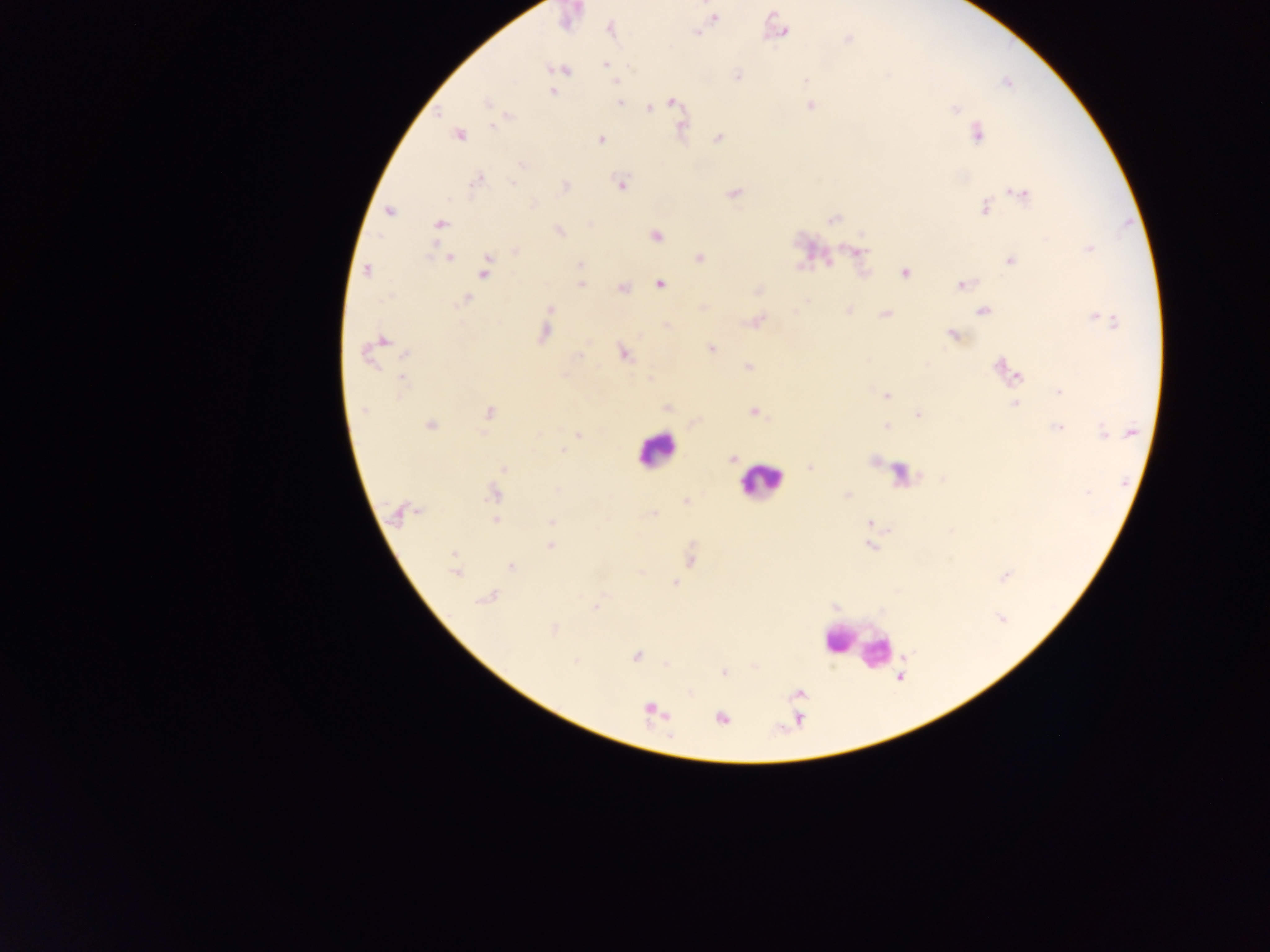

Plasmodium parasite locations = approximate centers as x y in pixels: 714 19; 610 30; 697 32; 782 32; 847 39; 606 64; 561 69; 736 76; 805 80; 616 81; 552 92; 619 102; 672 102; 485 103; 811 105; 649 108; 956 109; 494 126; 978 134; 459 136; 718 138; 601 140; 522 164; 476 181; 512 182; 621 184; 564 186; 734 193; 1019 194; 534 205; 985 207; 389 210; 833 220; 441 224; 590 225; 559 231; 656 235; 1090 248; 515 251; 857 251; 700 257; 449 258; 1010 261; 580 264; 366 271; 485 271; 905 273; 660 284; 581 285; 962 285; 623 288; 467 299; 550 309; 984 310; 885 314; 1104 319; 759 321; 667 325; 543 333; 953 335; 383 341; 711 349; 623 354; 365 355; 404 355; 749 367; 1002 367; 1014 374; 565 375; 402 379; 1059 391; 887 396; 1015 404; 667 408; 363 410; 489 412; 755 412; 918 414; 430 426; 887 426; 1058 428; 1115 431; 1103 433; 1130 433; 577 434; 562 450; 732 459; 503 468; 810 468; 1087 493; 493 494; 685 500; 397 514; 653 515; 496 521; 551 523; 869 523; 550 546; 870 546; 454 554; 690 560; 511 566; 455 573; 1004 576; 675 582; 486 598; 597 607; 1002 619; 554 630; 636 656; 575 661; 724 672; 652 710; 722 718
country = Ghana
image size = 1270×952 pixels
preparation = thick blood smear
leukocyte locations = approximate centers as x y in pixels: 654 450; 761 482; 857 646
field of view = single
capture = mobile-phone photograph through a microscope